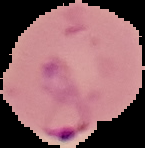
Malaria status: parasitized. Segmented cell region on a black background. From a thin blood smear. Image is 145×148 pixels.